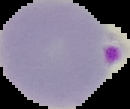

Segmented cell region on a black background. Malaria status: parasitized. From a thin blood film. Image is 130×109 pixels.